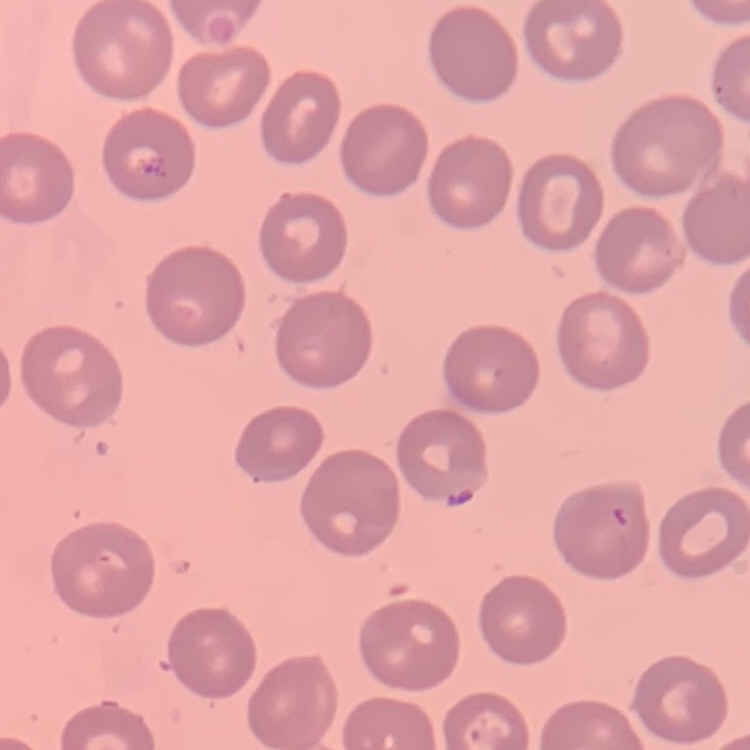
The red blood cells show no rouleaux formation. One tile cut from a larger photomicrograph. Stained with either Field's or Giemsa. Thin blood film.